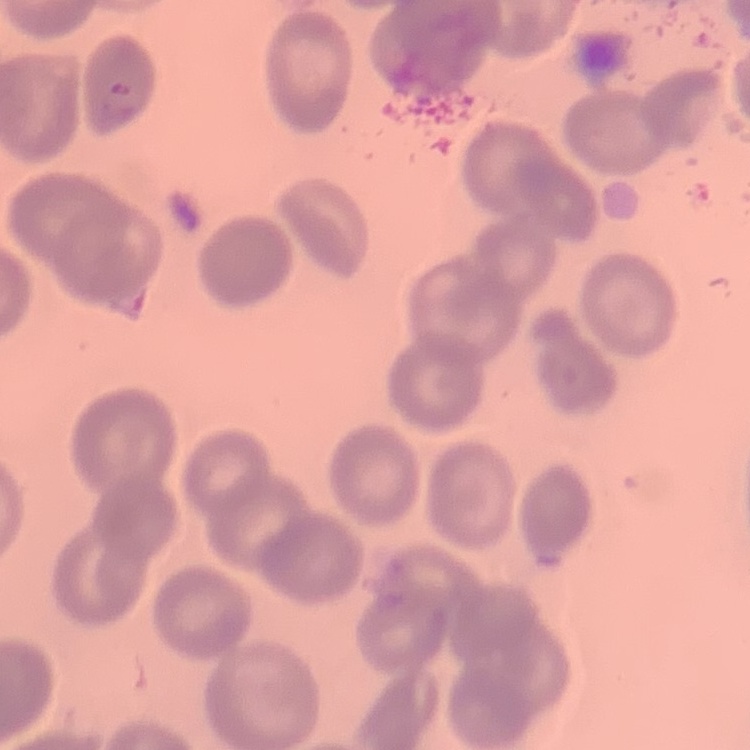
Summary:
  - Red blood cell morphology: no rouleaux formation
  - Stain: Field's or Giemsa
  - Preparation: thin blood smear
  - Image type: one tile cut from a larger photomicrograph